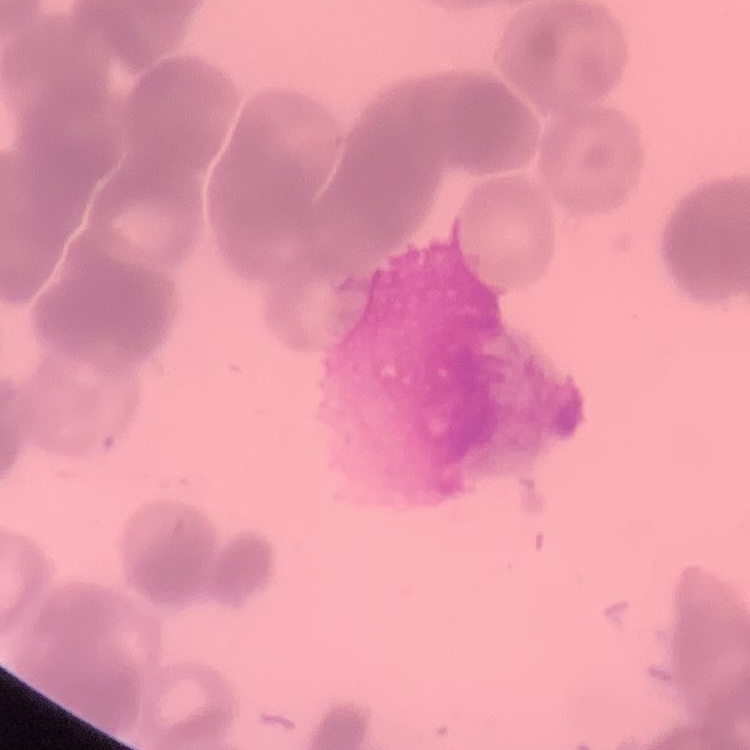
red blood cell morphology = rouleaux formation
image type = square crop of a larger photomicrograph
stain = Field's or Giemsa
preparation = thin blood film